Assess this cell for malaria.
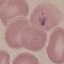
Uninfected.

stain: Giemsa
capture: smartphone through the microscope eyepiece
image_type: automatically extracted cell patch, resized to 64 × 64 pixels
preparation: thin blood smear